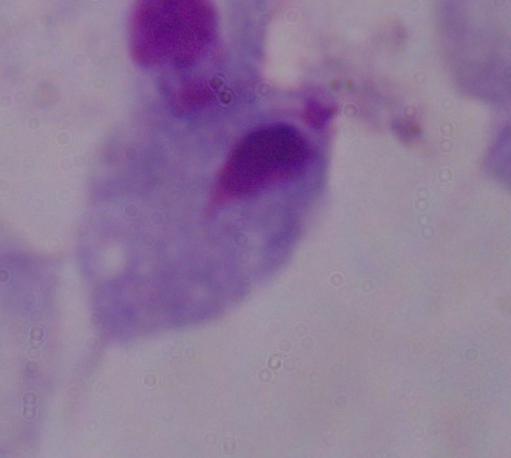 Photomicrograph. A trichomonad is seen. Captured at 1000x magnification.